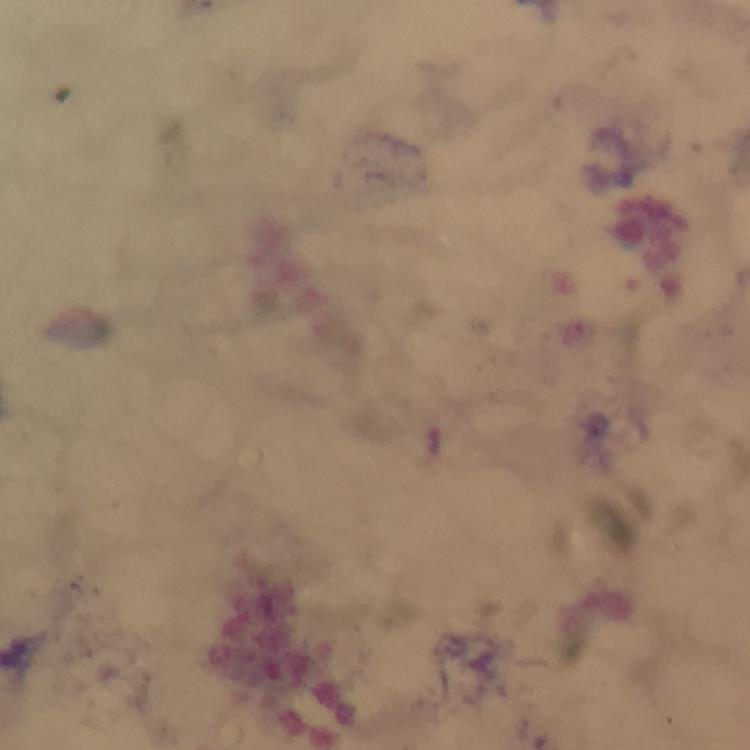

plasmodium_parasite_locations: 'approximate centers as (x, y) in pixels: (437, 441)'
magnification: 100x
immersion_oil: used
context: from a diagnostic examination for malaria
image_size: 750×750 pixels
stain: Giemsa
cropped_from: one field of view
capture: smartphone camera through the microscope
preparation: thick blood film